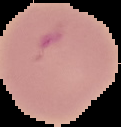
Summary:
  - Image type: cell region segmented out of the field of view; surrounding area masked to black
  - Malaria status: parasitized
  - Preparation: thin blood smear
  - Image size: 121×127 pixels